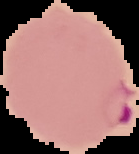

Summary:
  - Image type: cell region segmented out of the field of view; surrounding area masked to black
  - Image size: 139×154 pixels
  - Preparation: thin blood smear
  - Malaria status: parasitized